Point out each Plasmodium parasite.
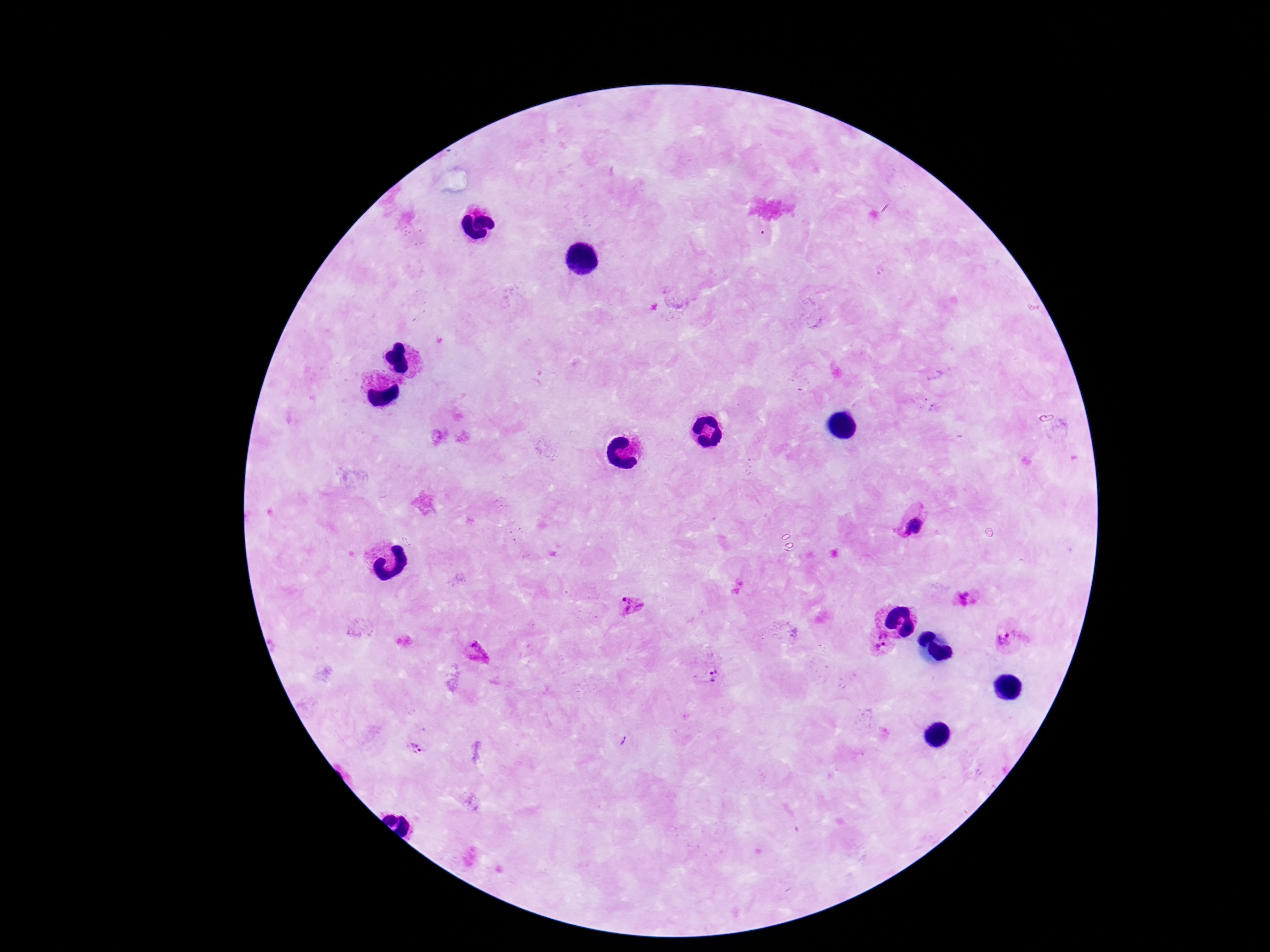

Approximate centers as [x, y] in pixels.
Plasmodium parasites: [914, 526], [964, 598], [632, 607], [1005, 638], [879, 642], [478, 653], [713, 674], [415, 749].

Patient malaria status: positive. 100x magnification. Thick blood smear. Image is 1270×952 pixels. One field from this slide. Smartphone photograph taken through the microscope eyepiece. Giemsa stain.